Assess this cell for malaria.
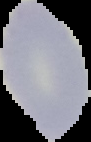
Uninfected.

image size = 91×142 pixels
preparation = thin blood smear
image type = cell region segmented out of the field of view; surrounding area masked to black